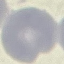

Result: no malaria parasites seen. Thin blood film. Giemsa-stained preparation. Automatically extracted cell patch, resized to 64 × 64 pixels. Photographed with a smartphone camera at the microscope eyepiece.